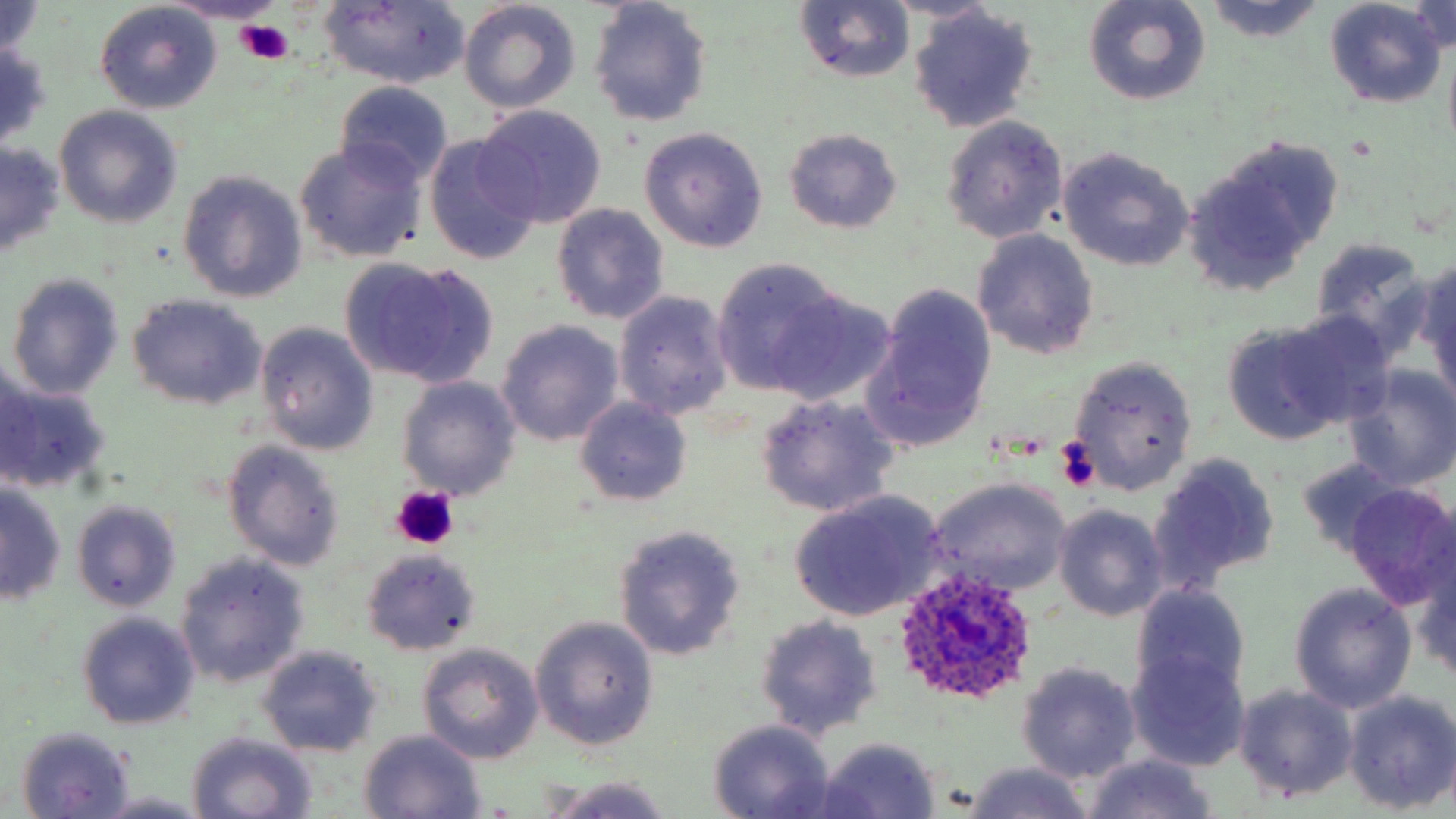 Approximate bounding boxes as named x1/y1/x2/y2 corners in pixels. Plasmodium ovale-infected red blood cell locations: (x1=892, y1=566, x2=1035, y2=708). Uninfected red blood cell locations: (x1=876, y1=0, x2=1003, y2=24), (x1=1085, y1=0, x2=1210, y2=106), (x1=1325, y1=0, x2=1446, y2=107), (x1=0, y1=1, x2=49, y2=64), (x1=587, y1=1, x2=713, y2=127), (x1=459, y1=2, x2=580, y2=113), (x1=794, y1=2, x2=916, y2=83), (x1=1203, y1=2, x2=1327, y2=44), (x1=95, y1=3, x2=222, y2=112), (x1=317, y1=3, x2=471, y2=87), (x1=1407, y1=3, x2=1456, y2=53), (x1=908, y1=7, x2=1040, y2=133), (x1=0, y1=41, x2=52, y2=149), (x1=334, y1=81, x2=454, y2=188), (x1=476, y1=105, x2=608, y2=227), (x1=54, y1=106, x2=182, y2=227), (x1=940, y1=115, x2=1069, y2=244), (x1=638, y1=127, x2=768, y2=252), (x1=782, y1=127, x2=903, y2=234), (x1=423, y1=135, x2=543, y2=266), (x1=293, y1=141, x2=427, y2=263), (x1=0, y1=143, x2=65, y2=255), (x1=1188, y1=144, x2=1339, y2=290), (x1=1057, y1=146, x2=1194, y2=272), (x1=179, y1=171, x2=308, y2=305), (x1=551, y1=204, x2=670, y2=324), (x1=971, y1=228, x2=1100, y2=361), (x1=1308, y1=238, x2=1437, y2=360), (x1=338, y1=257, x2=496, y2=383), (x1=711, y1=257, x2=847, y2=398), (x1=1414, y1=257, x2=1456, y2=405), (x1=7, y1=273, x2=123, y2=402), (x1=863, y1=283, x2=997, y2=450), (x1=757, y1=289, x2=900, y2=406), (x1=613, y1=291, x2=735, y2=420), (x1=127, y1=294, x2=266, y2=411), (x1=503, y1=306, x2=734, y2=431), (x1=1267, y1=312, x2=1398, y2=431), (x1=496, y1=320, x2=624, y2=447), (x1=1224, y1=320, x2=1350, y2=442), (x1=256, y1=323, x2=378, y2=454), (x1=1069, y1=355, x2=1198, y2=493), (x1=1345, y1=366, x2=1456, y2=490), (x1=396, y1=377, x2=521, y2=501), (x1=1, y1=380, x2=112, y2=495), (x1=754, y1=395, x2=902, y2=517), (x1=575, y1=398, x2=691, y2=506), (x1=221, y1=439, x2=345, y2=572), (x1=1147, y1=451, x2=1280, y2=590), (x1=1294, y1=457, x2=1401, y2=558), (x1=926, y1=478, x2=1072, y2=596), (x1=1343, y1=482, x2=1456, y2=608), (x1=1, y1=483, x2=66, y2=606), (x1=789, y1=492, x2=946, y2=620), (x1=72, y1=498, x2=181, y2=610), (x1=1054, y1=506, x2=1168, y2=621), (x1=614, y1=525, x2=747, y2=660), (x1=361, y1=548, x2=481, y2=656), (x1=175, y1=552, x2=309, y2=689), (x1=1411, y1=554, x2=1456, y2=685), (x1=1132, y1=583, x2=1252, y2=703), (x1=1289, y1=583, x2=1417, y2=713), (x1=77, y1=613, x2=200, y2=731), (x1=753, y1=614, x2=883, y2=740), (x1=529, y1=617, x2=659, y2=751), (x1=417, y1=642, x2=544, y2=764), (x1=257, y1=646, x2=384, y2=758), (x1=1127, y1=649, x2=1252, y2=771), (x1=1017, y1=661, x2=1142, y2=782), (x1=1232, y1=683, x2=1360, y2=802), (x1=1343, y1=690, x2=1456, y2=813), (x1=707, y1=720, x2=836, y2=817), (x1=14, y1=727, x2=137, y2=817), (x1=358, y1=730, x2=486, y2=817), (x1=186, y1=733, x2=316, y2=818), (x1=814, y1=738, x2=941, y2=817), (x1=1078, y1=754, x2=1219, y2=819), (x1=958, y1=763, x2=1094, y2=819), (x1=542, y1=775, x2=680, y2=818), (x1=93, y1=792, x2=214, y2=818). Platelet locations: (x1=238, y1=20, x2=296, y2=65), (x1=1056, y1=439, x2=1100, y2=492), (x1=391, y1=486, x2=458, y2=549). Slide-level diagnosis: Plasmodium ovale. 1000x magnification. Light microscopy. One field of a larger specimen. May-Grünwald-Giemsa-stained preparation. Image is 1456×819 pixels. Thin blood film.